Mark where platelets are.
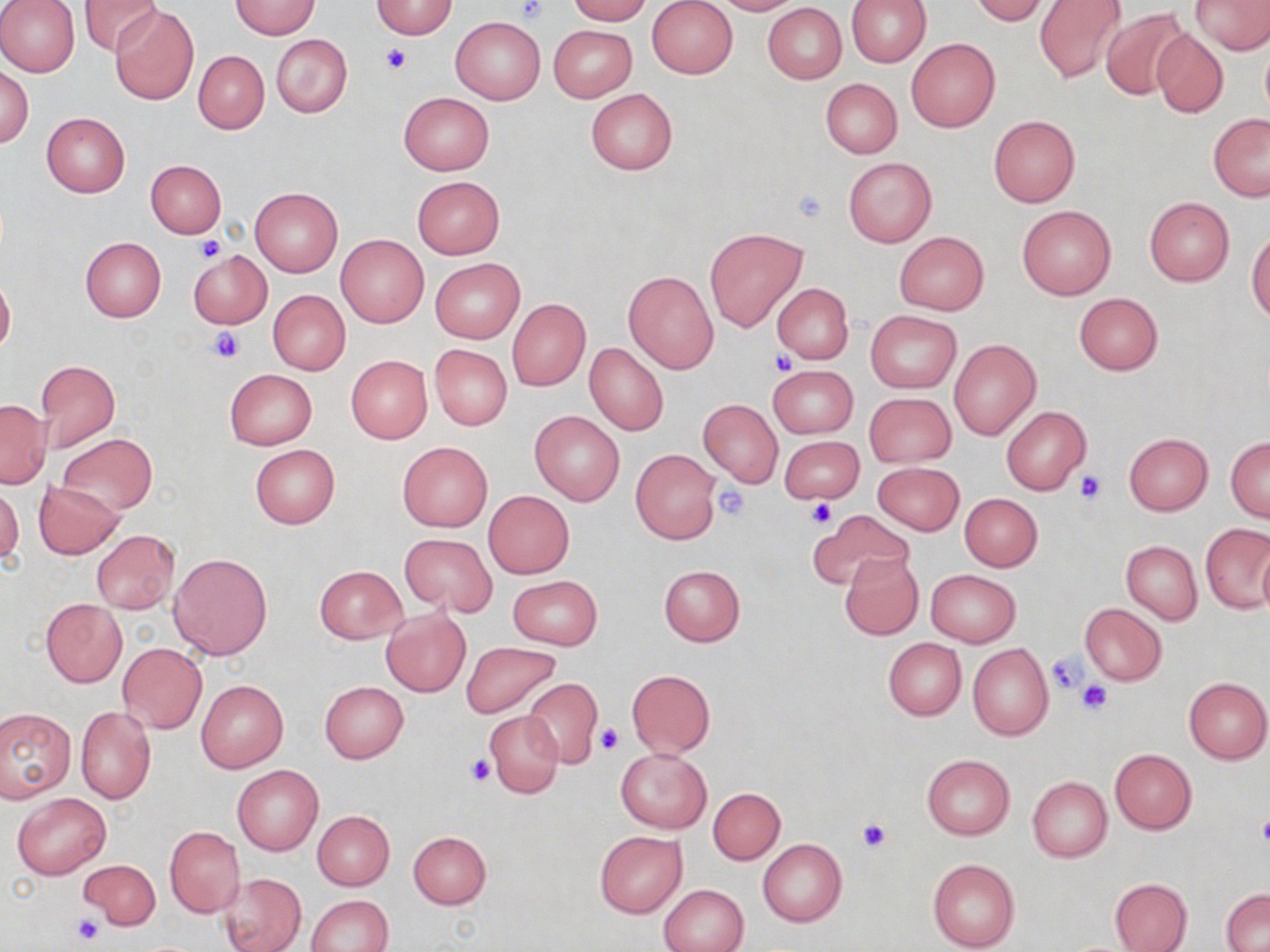

Approximate bounding boxes as (x1, y1, x2, y2) in pixels.
Platelets: (515, 0, 549, 23), (380, 43, 411, 75), (792, 187, 829, 223), (194, 235, 226, 264), (209, 328, 244, 363), (771, 349, 796, 376), (1076, 471, 1106, 504), (714, 485, 749, 521), (807, 499, 837, 528), (1045, 651, 1088, 695), (1075, 679, 1114, 717), (595, 725, 624, 756), (466, 756, 494, 787), (1257, 812, 1270, 849), (855, 819, 892, 854), (73, 915, 106, 946).

Uninfected red blood cell locations: (0, 0, 80, 78), (564, 0, 652, 24), (647, 0, 738, 79), (709, 0, 802, 15), (846, 0, 930, 67), (969, 0, 1049, 24), (1034, 0, 1127, 85), (1192, 0, 1270, 54), (79, 1, 163, 57), (230, 1, 319, 39), (371, 1, 458, 38), (762, 3, 846, 84), (110, 5, 201, 106), (1101, 7, 1190, 101), (450, 16, 545, 104), (548, 24, 637, 101), (1150, 26, 1228, 118), (272, 34, 352, 118), (907, 38, 1000, 132), (193, 50, 268, 134), (1, 65, 33, 149), (821, 78, 901, 158), (585, 88, 677, 174), (399, 91, 494, 175), (41, 112, 130, 198), (1208, 114, 1270, 200), (988, 115, 1080, 206), (843, 157, 937, 247), (146, 160, 226, 238), (412, 176, 504, 259), (250, 186, 343, 277), (1144, 197, 1235, 286), (1017, 206, 1116, 299), (704, 227, 808, 332), (1247, 230, 1270, 325), (894, 232, 988, 314), (336, 235, 429, 328), (80, 237, 166, 322), (187, 250, 272, 329), (431, 259, 523, 342), (623, 269, 719, 374), (0, 273, 15, 358), (773, 282, 853, 364), (267, 290, 351, 375), (1074, 292, 1162, 375), (507, 299, 589, 391), (865, 310, 961, 394), (947, 338, 1041, 440), (584, 341, 668, 436), (429, 344, 512, 430), (346, 355, 432, 444), (35, 359, 120, 455), (768, 365, 857, 438), (224, 368, 318, 450), (865, 392, 955, 467), (0, 399, 49, 487), (698, 400, 783, 487), (1002, 405, 1092, 495), (530, 410, 624, 506), (1123, 433, 1213, 515), (56, 434, 158, 515), (779, 435, 864, 505), (1226, 436, 1269, 522), (397, 441, 492, 531), (249, 443, 340, 529), (631, 449, 720, 544), (872, 461, 964, 535), (33, 481, 124, 558), (0, 482, 22, 569), (484, 491, 574, 579), (959, 493, 1043, 572), (810, 509, 913, 593), (1201, 524, 1269, 613), (91, 530, 179, 613), (399, 532, 497, 616), (1121, 541, 1202, 624), (1257, 547, 1270, 620), (168, 551, 274, 660), (839, 553, 924, 642), (659, 564, 745, 646), (313, 565, 407, 643), (925, 569, 1020, 648), (507, 574, 603, 651), (40, 599, 126, 687), (1080, 604, 1167, 685), (381, 608, 472, 697), (883, 638, 966, 720), (461, 641, 562, 719), (118, 643, 207, 733), (967, 644, 1053, 741), (627, 669, 715, 757), (1184, 676, 1270, 764), (521, 678, 603, 769), (196, 680, 288, 773), (319, 681, 408, 764), (0, 706, 75, 800), (75, 706, 156, 804), (486, 711, 565, 799), (615, 748, 711, 833), (1109, 749, 1197, 833), (921, 754, 1015, 839), (232, 764, 324, 855), (1026, 776, 1112, 863), (708, 787, 785, 864), (12, 793, 110, 880), (311, 810, 394, 890), (164, 826, 245, 916), (408, 830, 491, 909), (594, 832, 687, 919), (758, 839, 846, 926), (77, 859, 161, 929), (927, 859, 1019, 952), (218, 872, 306, 952), (1110, 878, 1192, 952), (659, 884, 748, 951), (1221, 888, 1270, 950), (307, 894, 392, 952). Slide-level diagnosis: no evidence of blood parasites. Image is 1270×952 pixels. Captured at 1000x magnification. May-Grünwald-Giemsa stain. One field of a larger specimen. Light microscopy. Thin blood film.